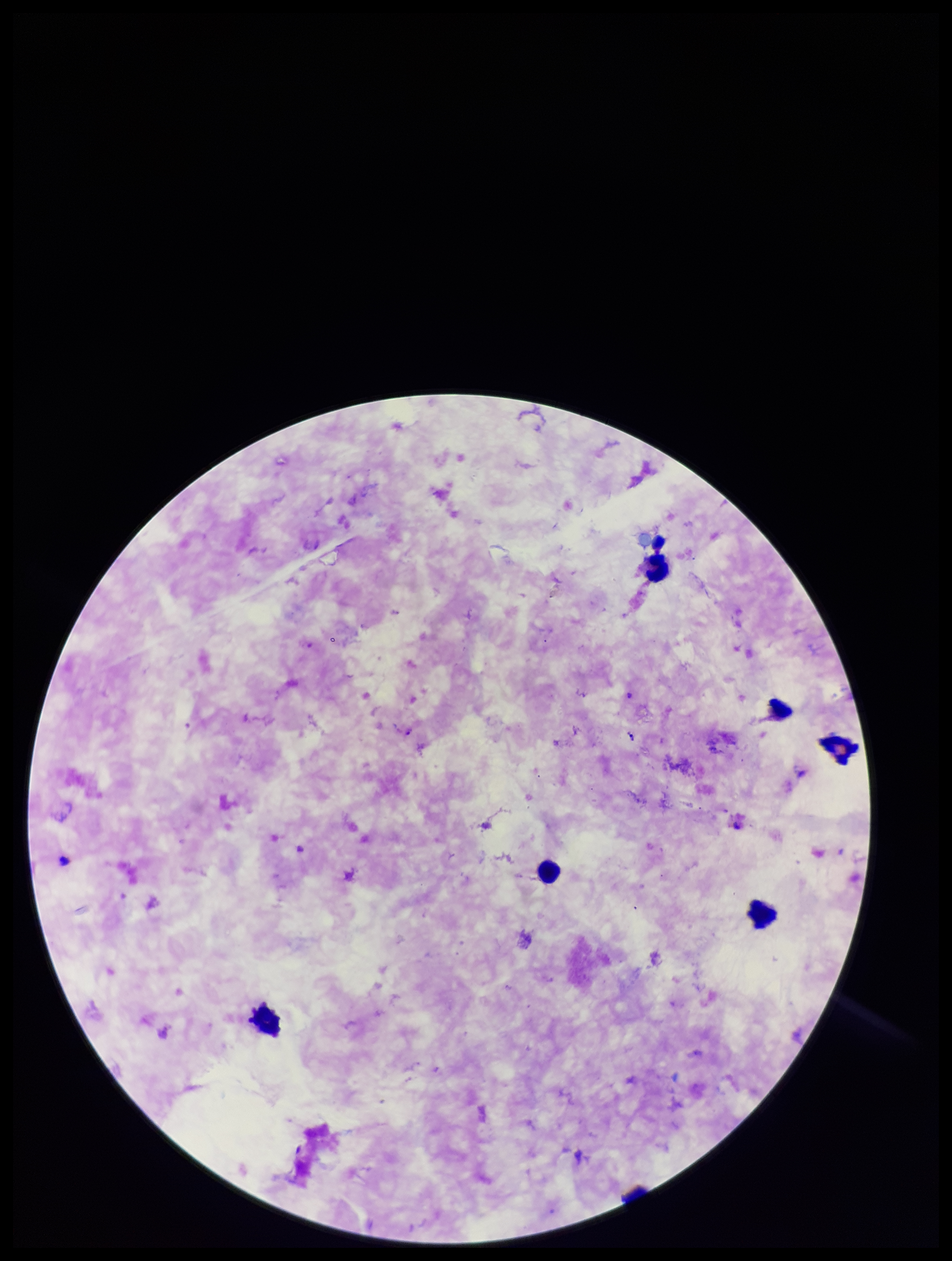 Stained with Giemsa. Plasmodium parasites: identified. Parasite count: 1. Patient malaria status: positive. One field from this slide. Leukocyte count: 6. Image is 952×1261 pixels. Preparation: thick blood smear. Species reported for this patient: Plasmodium falciparum. Photographed through the microscope eyepiece with a smartphone camera.